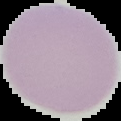

Summary:
  - Image type: cell region segmented out of the field of view; surrounding area masked to black
  - Preparation: thin blood film
  - Malaria status: uninfected
  - Image size: 121×121 pixels